Name the blood parasite species.
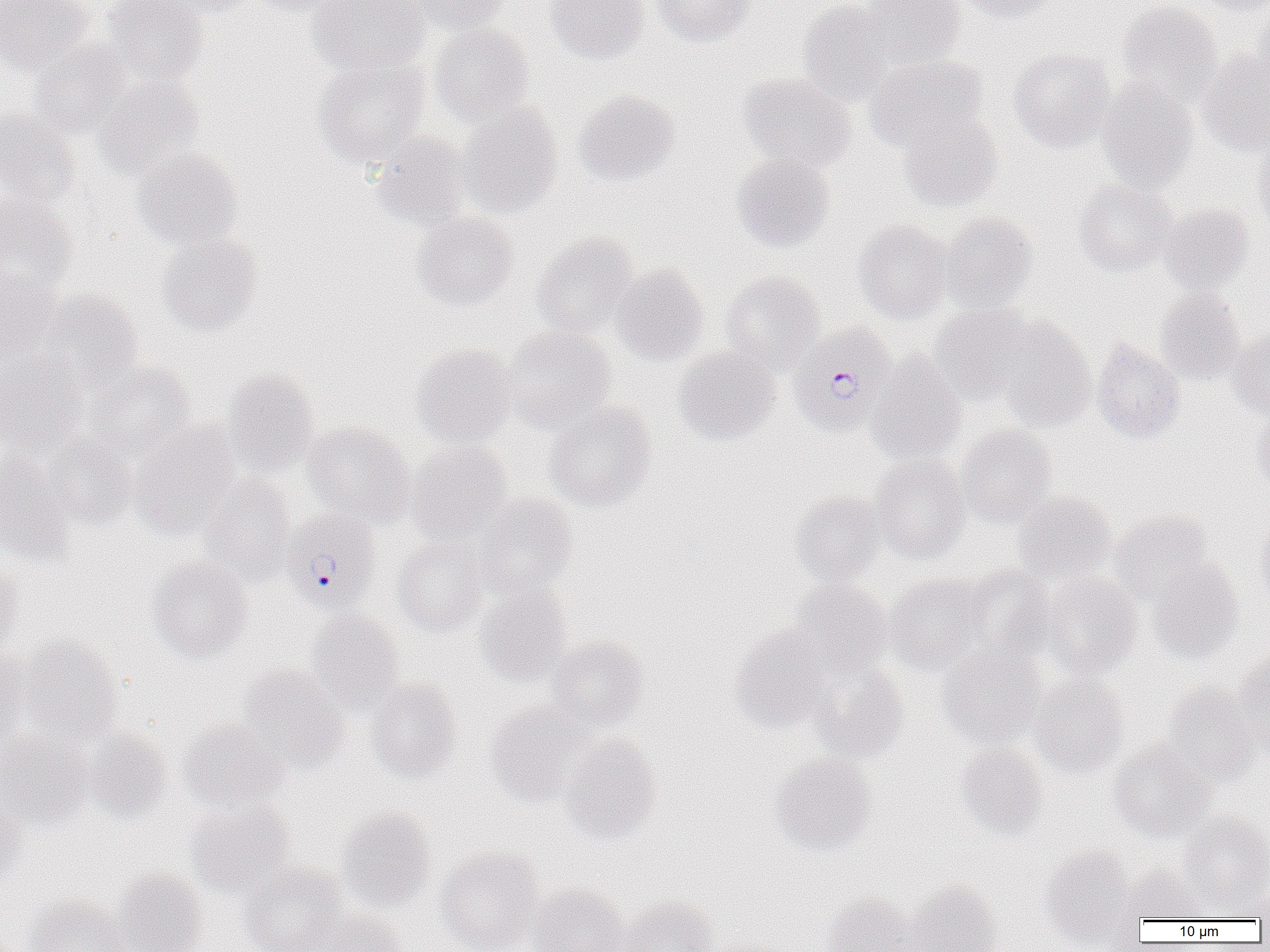

Plasmodium falciparum.

Summary:
  - Coordinate format: approximate bounding boxes as [x1, y1, x2, y2] in pixels
  - Plasmodium falciparum-infected red blood cell locations: [789, 323, 897, 437], [279, 509, 381, 614]
  - Uninfected red blood cell locations: [0, 0, 92, 73], [101, 0, 209, 84], [157, 0, 257, 17], [243, 0, 347, 16], [309, 0, 429, 77], [410, 0, 510, 35], [546, 0, 649, 64], [650, 0, 755, 47], [861, 0, 965, 69], [956, 0, 1056, 23], [1192, 0, 1270, 16], [797, 1, 894, 106], [1117, 2, 1222, 108], [1250, 4, 1270, 94], [430, 24, 534, 125], [29, 39, 131, 137], [1008, 47, 1114, 151], [1198, 49, 1270, 155], [866, 56, 988, 151], [314, 57, 430, 169], [738, 73, 856, 174], [91, 77, 205, 180], [1096, 80, 1198, 193], [574, 89, 681, 186], [456, 102, 563, 218], [0, 105, 80, 205], [898, 114, 1002, 211], [372, 133, 475, 230], [1253, 133, 1270, 236], [133, 148, 243, 250], [731, 154, 834, 252], [1073, 179, 1177, 277], [0, 191, 77, 289], [1158, 204, 1253, 293], [411, 211, 518, 312], [939, 212, 1038, 314], [853, 220, 953, 324], [156, 232, 262, 335], [531, 232, 639, 338], [611, 263, 709, 366], [0, 264, 61, 359], [719, 271, 825, 373], [38, 289, 142, 391], [1155, 289, 1245, 382], [930, 304, 1034, 403], [991, 316, 1097, 430], [501, 326, 616, 431], [1228, 329, 1270, 417], [1091, 339, 1185, 443], [411, 343, 515, 447], [673, 346, 780, 446], [0, 348, 86, 453], [866, 352, 967, 467], [88, 362, 197, 462], [222, 370, 319, 477], [544, 401, 657, 512], [1250, 407, 1270, 495], [303, 421, 416, 525], [955, 423, 1057, 528], [130, 424, 241, 539], [42, 434, 138, 529], [406, 441, 513, 545], [0, 453, 74, 565], [871, 455, 972, 565], [197, 475, 295, 584], [790, 490, 887, 586], [1012, 491, 1116, 585], [472, 493, 577, 594], [1109, 508, 1216, 601], [1254, 512, 1270, 608], [392, 535, 490, 636], [0, 555, 23, 657], [146, 557, 253, 663], [1147, 559, 1244, 661], [960, 566, 1056, 666], [884, 572, 994, 676], [1036, 573, 1143, 677], [789, 579, 892, 676], [474, 584, 573, 687], [306, 608, 404, 711], [730, 625, 833, 734], [546, 635, 650, 731], [18, 637, 122, 742], [938, 644, 1046, 747], [0, 651, 34, 750], [1232, 653, 1270, 756], [810, 663, 909, 760], [238, 666, 349, 769], [1028, 673, 1129, 778], [365, 677, 463, 782], [1161, 681, 1261, 786], [485, 702, 596, 806], [178, 718, 290, 813], [84, 729, 172, 823], [0, 731, 91, 830], [559, 734, 661, 843], [1108, 740, 1215, 842], [955, 741, 1048, 839], [771, 754, 877, 856], [0, 794, 28, 886], [189, 803, 298, 900], [337, 806, 438, 913], [1178, 810, 1270, 909], [438, 846, 544, 952], [1041, 847, 1139, 948], [239, 861, 349, 952], [1125, 866, 1209, 922], [114, 868, 209, 952], [1230, 877, 1270, 922], [905, 880, 1002, 952], [1248, 883, 1270, 924], [529, 884, 629, 952], [821, 892, 914, 952], [26, 894, 132, 952], [621, 897, 718, 952], [318, 911, 406, 952]
  - Image size: 1270×952 pixels
  - Modality: light microscopy
  - Magnification: 1000x
  - Preparation: thin blood film
  - Field of view: single